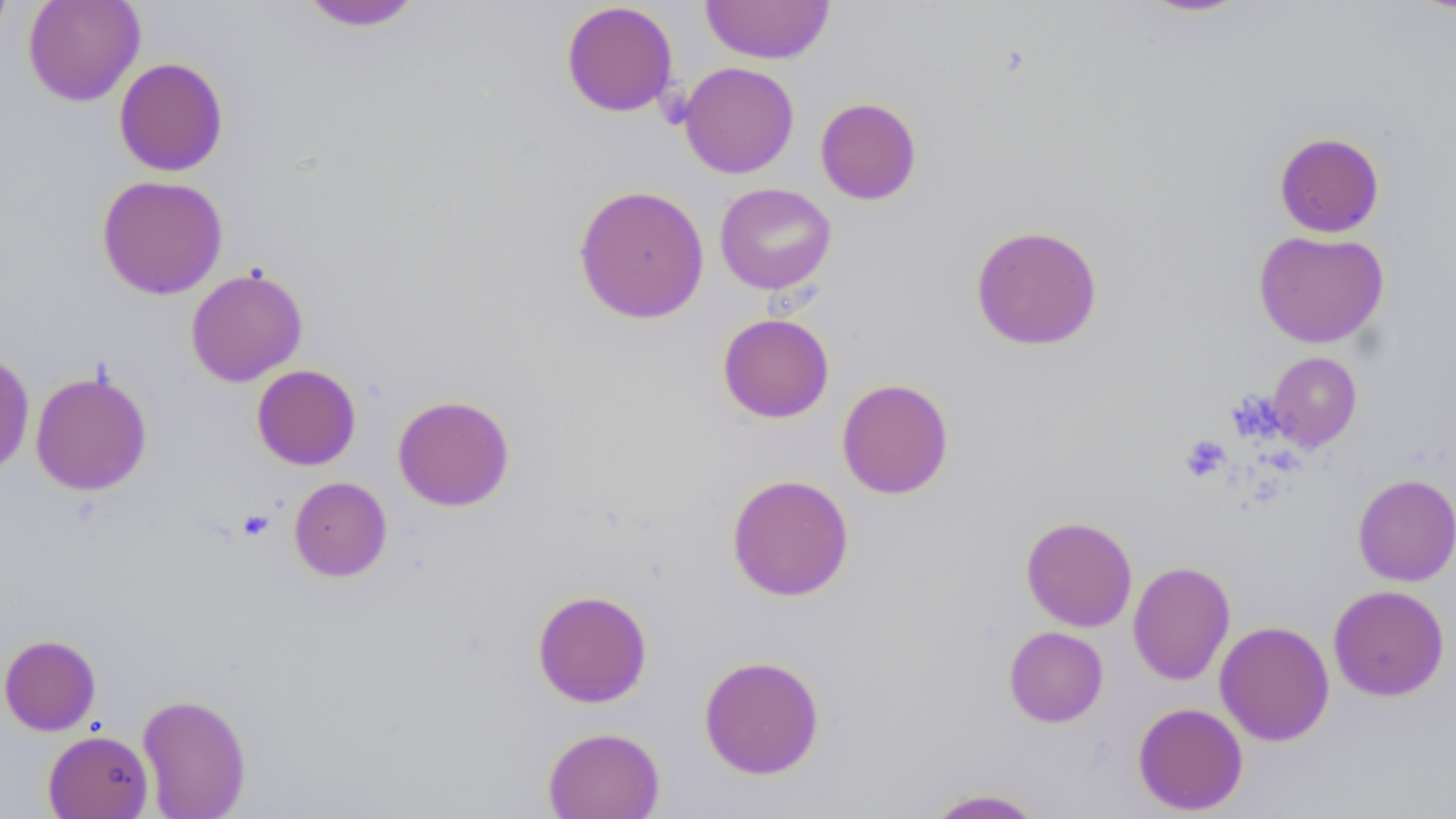
Approximate bounding boxes as named x1/y1/x2/y2 corners in pixels. Platelet locations: (x1=1180, y1=435, x2=1231, y2=482), (x1=238, y1=509, x2=274, y2=541). Uninfected red blood cell locations: (x1=0, y1=0, x2=13, y2=48), (x1=23, y1=0, x2=145, y2=106), (x1=700, y1=0, x2=835, y2=64), (x1=1134, y1=0, x2=1254, y2=18), (x1=296, y1=1, x2=426, y2=32), (x1=561, y1=1, x2=678, y2=117), (x1=113, y1=57, x2=229, y2=177), (x1=678, y1=61, x2=799, y2=178), (x1=815, y1=97, x2=922, y2=205), (x1=1274, y1=132, x2=1385, y2=238), (x1=96, y1=175, x2=229, y2=300), (x1=715, y1=182, x2=836, y2=295), (x1=572, y1=184, x2=710, y2=324), (x1=970, y1=224, x2=1103, y2=351), (x1=1253, y1=229, x2=1389, y2=348), (x1=186, y1=267, x2=308, y2=387), (x1=718, y1=313, x2=835, y2=423), (x1=0, y1=349, x2=35, y2=477), (x1=1266, y1=352, x2=1362, y2=452), (x1=251, y1=364, x2=361, y2=470), (x1=30, y1=370, x2=152, y2=496), (x1=836, y1=378, x2=954, y2=499), (x1=392, y1=394, x2=515, y2=511), (x1=726, y1=473, x2=854, y2=601), (x1=1352, y1=473, x2=1456, y2=586), (x1=289, y1=476, x2=392, y2=581), (x1=1020, y1=515, x2=1138, y2=631), (x1=1128, y1=560, x2=1235, y2=686), (x1=1328, y1=584, x2=1450, y2=701), (x1=532, y1=590, x2=653, y2=707), (x1=1214, y1=621, x2=1334, y2=746), (x1=1003, y1=626, x2=1108, y2=727), (x1=0, y1=634, x2=101, y2=736), (x1=698, y1=654, x2=825, y2=779), (x1=136, y1=693, x2=252, y2=818), (x1=1133, y1=702, x2=1248, y2=815), (x1=542, y1=726, x2=665, y2=819), (x1=42, y1=730, x2=154, y2=818), (x1=923, y1=787, x2=1046, y2=818). Slide-level diagnosis: no evidence of blood parasites. May-Grünwald-Giemsa stain. Thin blood film. Image is 1456×819 pixels. One field of a larger specimen. Light microscopy. Captured at 1000x magnification.